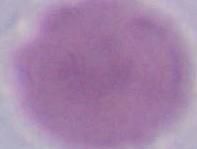
modality = micrograph
identification = erythrocyte
magnification = 1000x